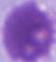

A red blood cell is seen. Captured at 1000x magnification. Photomicrograph.